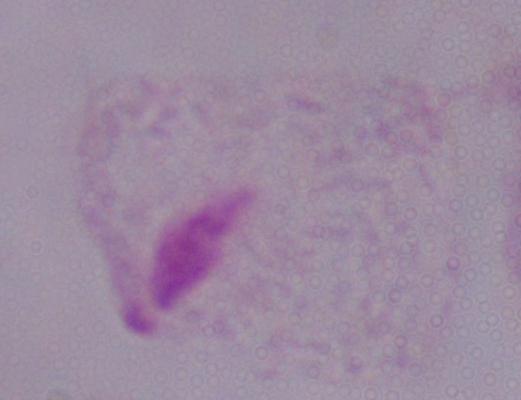
{
  "modality": "micrograph",
  "identification": "trichomonad",
  "magnification": "1000x"
}